Locate and identify every blood parasite.
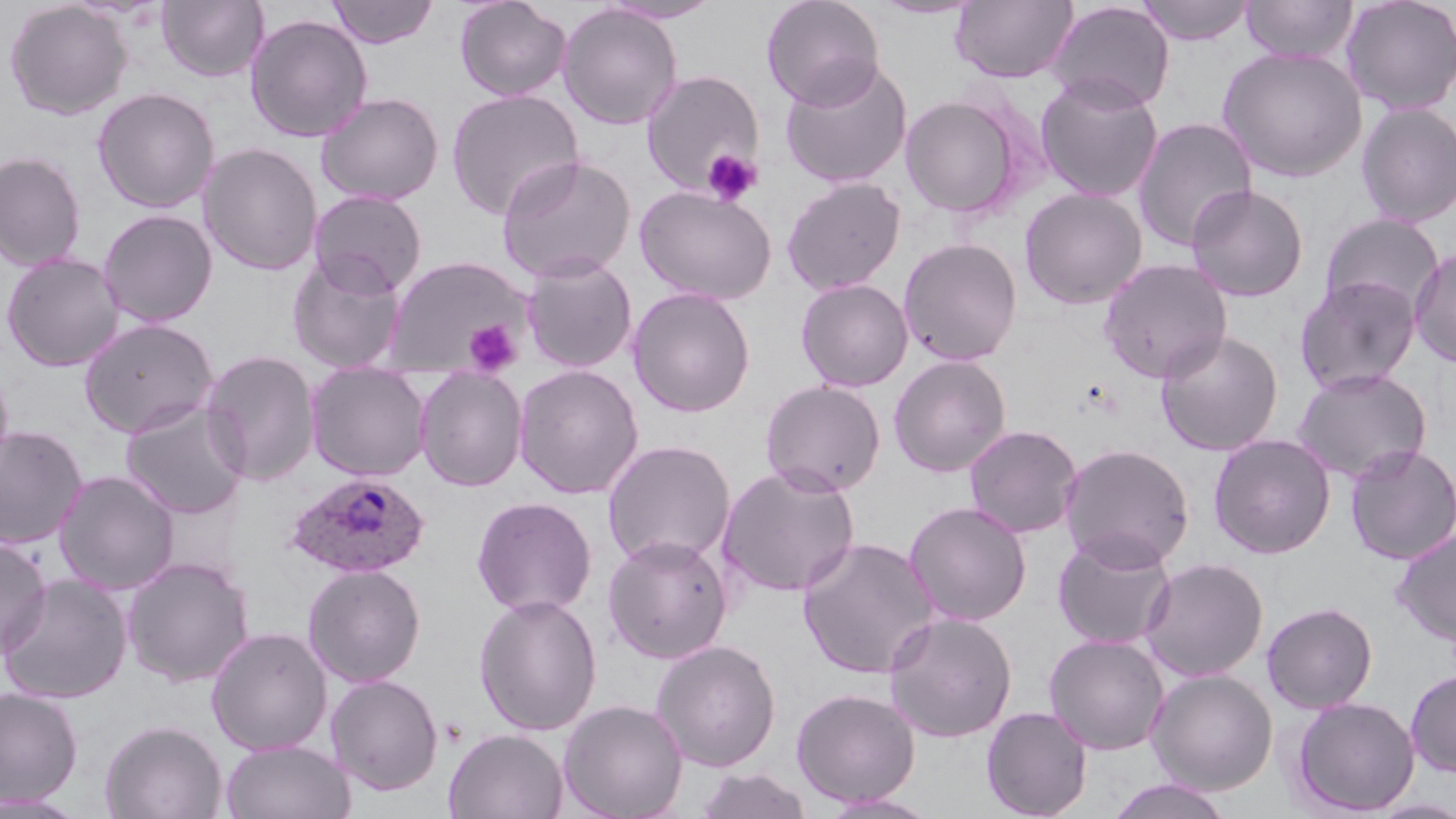

Approximate bounding boxes as (x1,y1)-(x2,y2) corner pairs in pixels.
Plasmodium ovale-infected red blood cells: (285,472)-(431,579).
No Plasmodium falciparum, Plasmodium malariae, Plasmodium vivax, Babesia divergens, or Trypanosoma brucei observed.

slide_level_diagnosis: Plasmodium ovale
uninfected_red_blood_cell_locations: 'approximate bounding boxes as (x1,y1)-(x2,y2) corner pairs in pixels: (156,0)-(269,83), (327,0)-(438,48), (454,0)-(572,102), (599,0)-(723,24), (761,0)-(885,109), (870,0)-(984,20), (950,0)-(1079,84), (1137,0)-(1255,45), (1241,0)-(1358,64), (1340,0)-(1456,115), (3,1)-(133,120), (1046,1)-(1174,113), (557,4)-(683,130), (244,14)-(373,143), (1217,46)-(1368,182), (779,58)-(913,189), (641,70)-(764,196), (1035,74)-(1164,203), (92,87)-(220,214), (446,89)-(584,220), (316,91)-(444,206), (900,94)-(1024,219), (1355,101)-(1456,228), (1131,117)-(1258,252), (198,142)-(323,276), (0,151)-(87,273), (495,153)-(637,283), (782,177)-(906,295), (634,184)-(777,305), (1186,184)-(1309,302), (1019,187)-(1148,310), (308,190)-(428,296), (97,208)-(219,328), (1320,212)-(1445,321), (898,237)-(1023,366), (1409,247)-(1456,368), (1,251)-(125,372), (287,252)-(407,373), (383,255)-(532,377), (521,255)-(638,373), (1097,258)-(1233,383), (1294,275)-(1422,395), (795,278)-(914,392), (627,286)-(757,418), (78,317)-(220,438), (1155,330)-(1284,456), (200,349)-(320,485), (888,354)-(1012,477), (305,362)-(432,481), (0,363)-(15,482), (513,364)-(645,499), (414,366)-(528,492), (1292,368)-(1432,483), (759,380)-(886,497), (120,401)-(250,520), (963,424)-(1083,539), (0,425)-(88,550), (1208,434)-(1336,559), (602,440)-(737,569), (1058,442)-(1195,571), (1344,443)-(1456,565), (716,463)-(861,598), (53,470)-(180,595), (471,497)-(597,617), (903,501)-(1032,627), (1390,528)-(1456,647), (1052,531)-(1177,650), (0,534)-(52,659), (602,534)-(734,664), (798,536)-(939,680), (122,556)-(255,687), (1139,557)-(1269,682), (303,563)-(427,687), (1,574)-(134,705), (474,593)-(602,736), (1261,601)-(1378,713), (882,611)-(1018,743), (206,626)-(333,756), (1044,634)-(1170,755), (650,639)-(782,772), (1146,669)-(1278,795), (1405,669)-(1456,777), (325,673)-(444,795), (0,686)-(83,806), (791,688)-(921,807), (1291,696)-(1420,816), (557,698)-(688,819), (981,706)-(1092,819), (99,719)-(227,819), (443,728)-(568,819), (220,739)-(356,819), (694,766)-(813,819), (1105,778)-(1236,819), (0,792)-(92,817), (818,792)-(942,818)'
platelet_locations: 'approximate bounding boxes as (x1,y1)-(x2,y2) corner pairs in pixels: (701,148)-(762,206), (463,319)-(522,375)'
image_size: 1456×819 pixels
magnification: 1000x
preparation: thin blood smear
field_of_view: one of a larger specimen
stain: May-Grünwald-Giemsa
modality: optical microscopy